Identify the parasite.
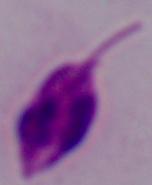

Leishmania.

Captured at 1000x magnification. Photomicrograph.